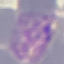

Summary:
  - Malaria status: parasitized
  - Preparation: thin blood smear
  - Image type: automatically extracted cell patch, resized to 64 × 64 pixels
  - Capture: smartphone through the microscope eyepiece
  - Stain: Giemsa